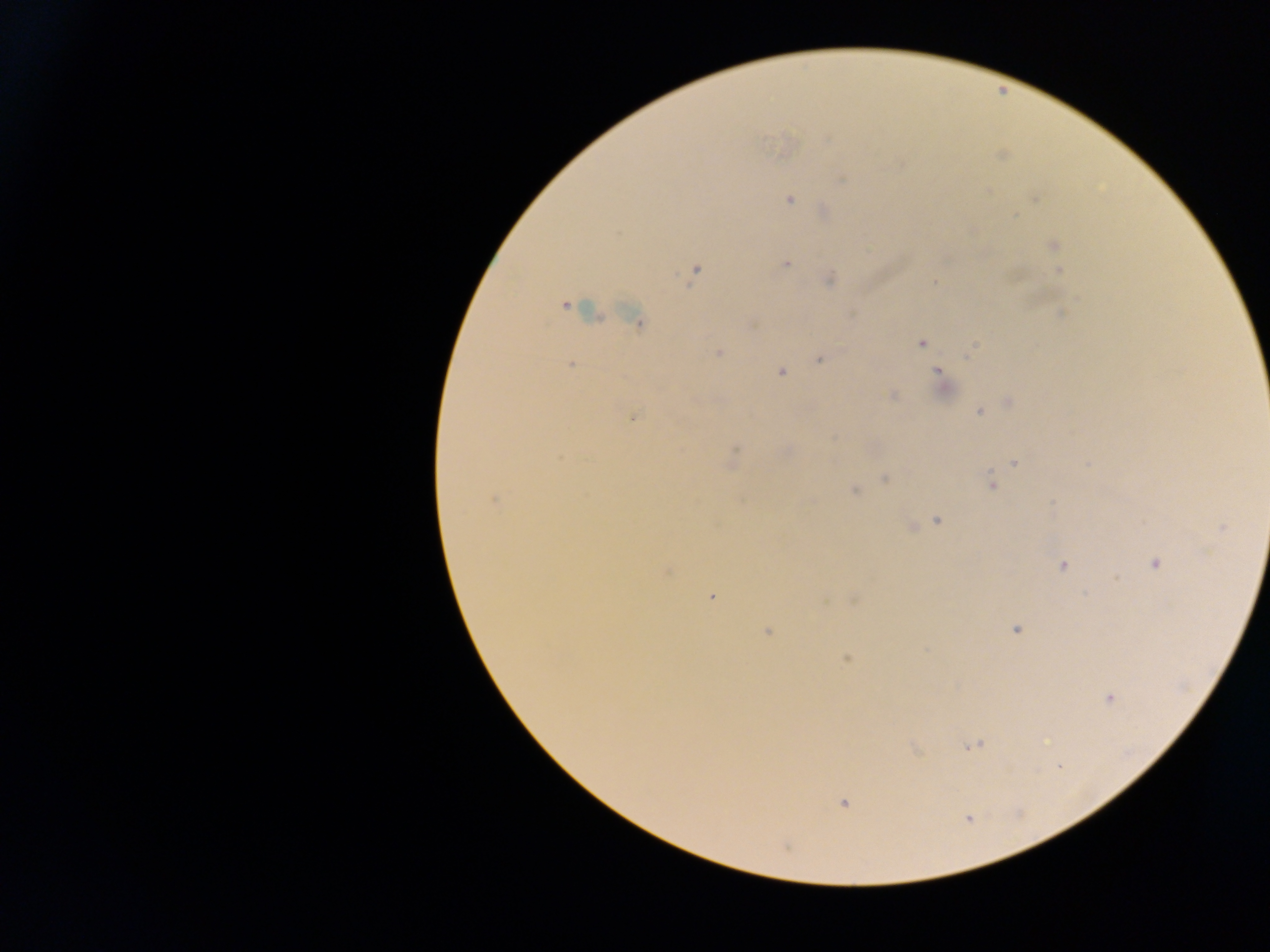

Approximate centers as (x, y) in pixels. Plasmodium parasite locations: (828, 140), (841, 180), (988, 191), (789, 199), (1035, 199), (1015, 217), (1053, 245), (786, 263), (695, 271), (1059, 271), (829, 279), (934, 283), (565, 306), (570, 307), (1062, 313), (636, 320), (922, 342), (971, 350), (718, 353), (819, 359), (571, 365), (780, 372), (938, 372), (892, 395), (1009, 403), (979, 412), (634, 417), (735, 449), (1014, 462), (885, 478), (992, 485), (854, 490), (494, 500), (937, 520), (911, 527), (1222, 528), (1156, 563), (1063, 566), (711, 596), (854, 599), (1016, 629), (767, 632), (846, 658), (1109, 698), (974, 746), (1059, 766), (843, 802). Collected in Ghana. Single field of view. Image is 1270×952 pixels. Mobile-phone photograph taken through the microscope. Thick blood smear.